Assess this cell for malaria.
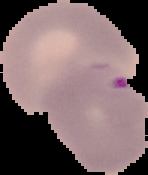

It is parasitized.

image type = segmented cell region on a black background
preparation = thin blood film
image size = 148×175 pixels